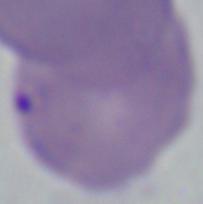 A Babesia parasite is seen. 1000x magnification. Micrograph.